Identify the preparation type.
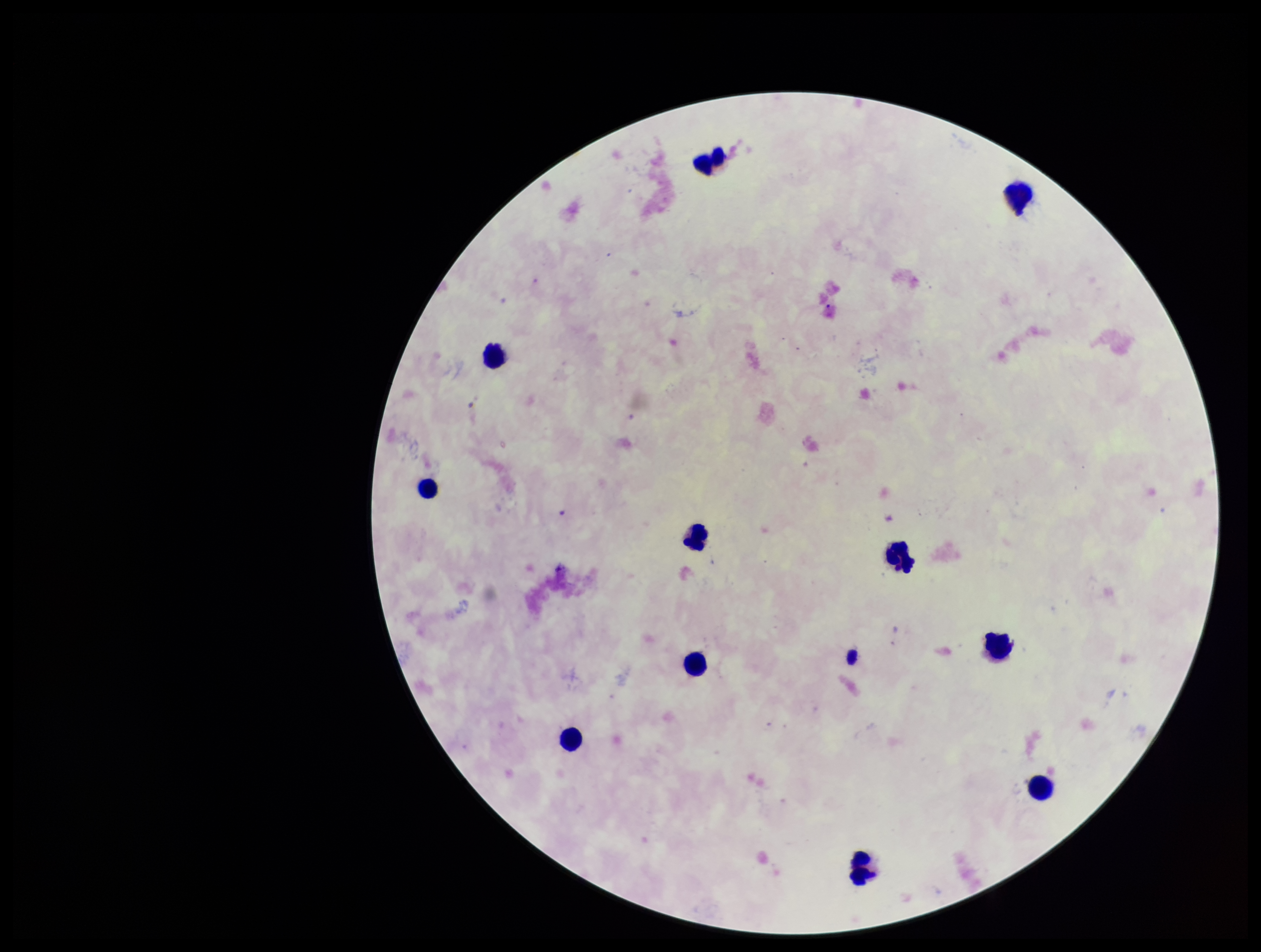
Thick.

Smartphone photograph taken through the eyepiece of a microscope. Patient malaria status: negative. Leukocyte count: 11. Single field of view. Plasmodium parasites: none detected. Parasite count: 0. Stained with Giemsa. Image is 1261×952 pixels.